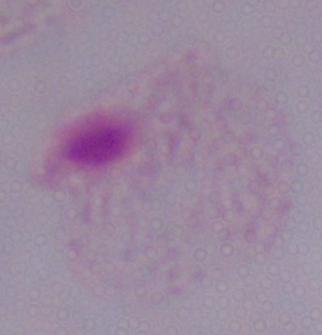

Captured at 1000x magnification. Micrograph. A trichomonad is shown.